Give the position of each Plasmodium falciparum parasite with its life-cycle stage, each leukocyte, and any debris.
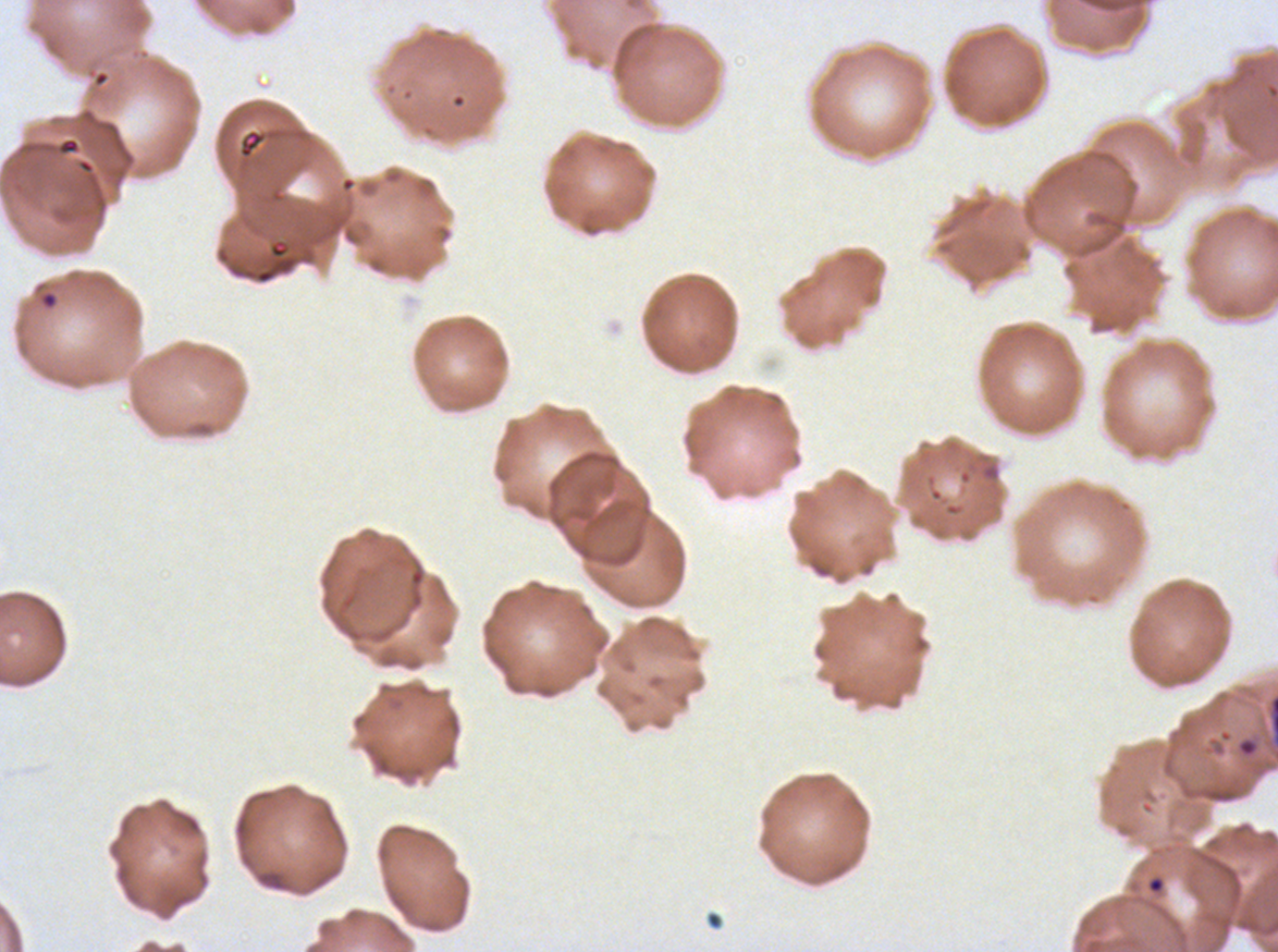

Approximate bounding rectangles given as corner coordinates in pixels from the top-left.
Rings: (x1=38, y1=289, x2=59, y2=311), (x1=1147, y1=875, x2=1165, y2=895).
Debris: (x1=57, y1=137, x2=80, y2=155), (x1=1237, y1=738, x2=1257, y2=757).
No late-ring/early-trophozoite forms, mid trophozoites, late trophozoites, early schizonts, late schizonts, segmenters, gametocytes, or leukocytes observed.

Summary:
  - Preparation: thin blood smear
  - Specimen: ex-vivo Plasmodium falciparum culture from a patient in The Gambia, grown for 24 to 48 hours
  - Image size: 1278×952 pixels
  - Stain: Giemsa
  - Field of view: one sub-image of a larger composite